Locate and identify every blood parasite.
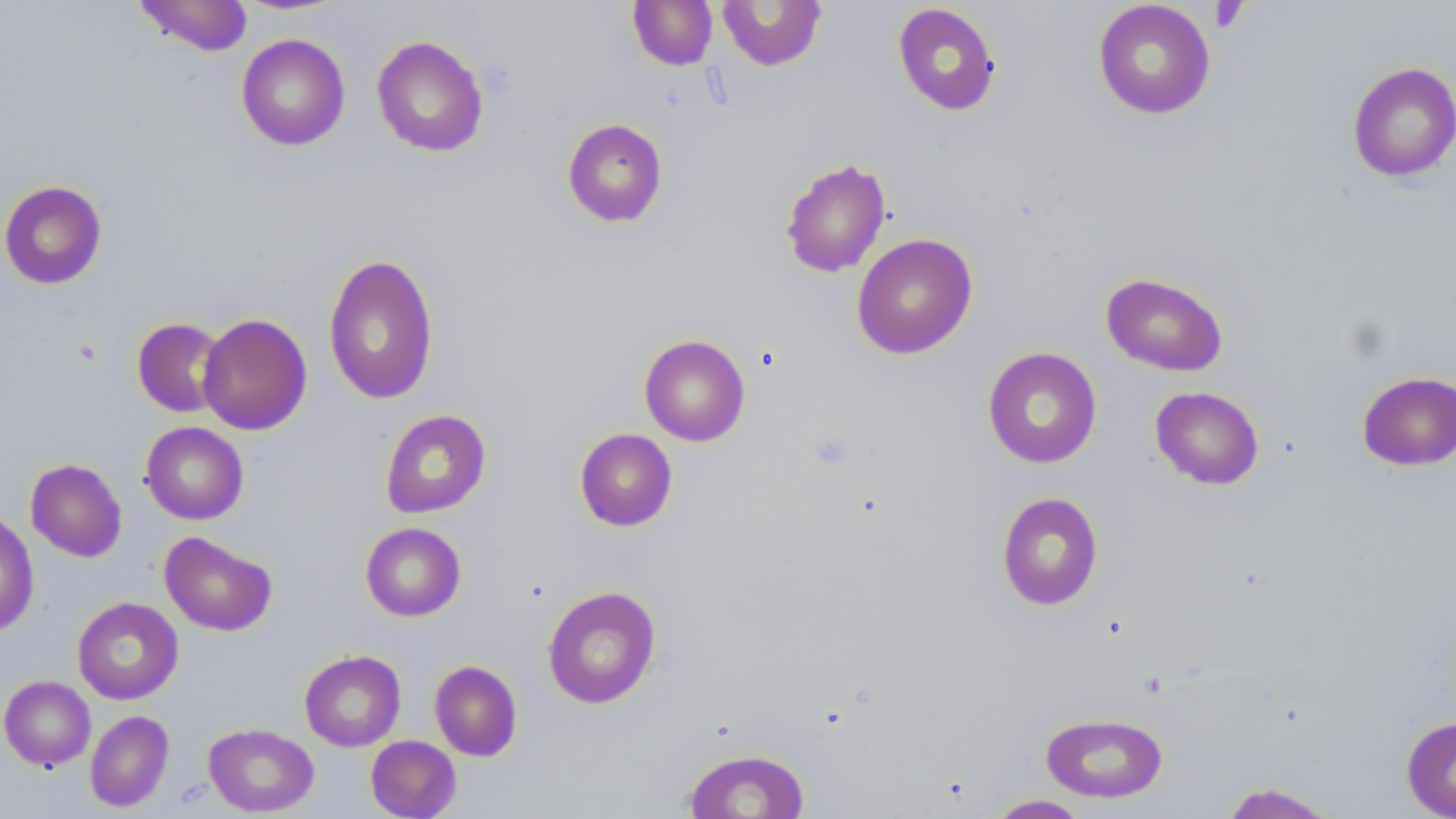
No blood parasites observed.

Summary:
  - Coordinate format: approximate bounding boxes as [x1, y1, x2, y2] in pixels
  - Uninfected red blood cell locations: [134, 0, 253, 56], [718, 0, 827, 71], [1092, 0, 1216, 119], [628, 1, 718, 70], [893, 2, 1001, 116], [236, 33, 350, 151], [371, 35, 488, 157], [1346, 61, 1456, 182], [562, 118, 668, 227], [779, 157, 891, 278], [0, 180, 107, 289], [851, 233, 978, 359], [322, 252, 439, 406], [1101, 272, 1228, 376], [197, 313, 312, 435], [132, 317, 228, 418], [639, 334, 750, 446], [983, 347, 1102, 468], [1356, 371, 1456, 471], [1150, 386, 1264, 489], [380, 409, 491, 518], [140, 422, 248, 524], [574, 428, 677, 531], [25, 458, 127, 562], [997, 492, 1104, 610], [0, 511, 39, 637], [360, 522, 466, 621], [159, 531, 277, 636], [542, 586, 660, 709], [72, 597, 184, 705], [299, 649, 406, 751], [430, 660, 522, 761], [0, 675, 96, 771], [85, 710, 174, 812], [1040, 712, 1168, 803], [1401, 716, 1456, 818], [204, 723, 318, 816], [365, 735, 461, 819], [682, 748, 810, 818], [1220, 782, 1340, 818], [985, 794, 1090, 818]
  - Platelet locations: [1210, 1, 1248, 33], [810, 432, 854, 470]
  - Slide-level diagnosis: negative for blood parasites
  - Image size: 1456×819 pixels
  - Modality: optical microscopy
  - Preparation: thin blood film
  - Field of view: single
  - Stain: May-Grünwald-Giemsa
  - Magnification: 1000x